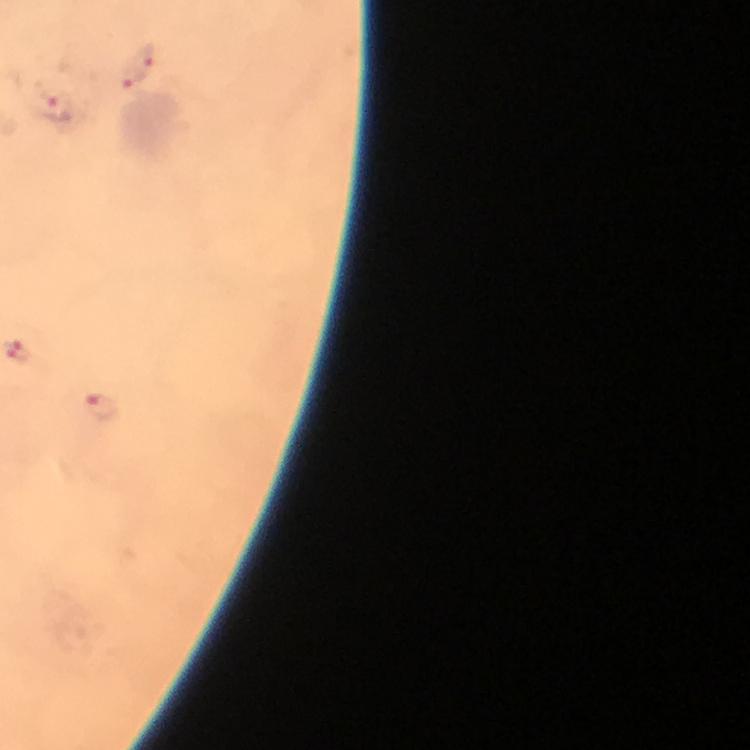
Approximate centers as [x, y] in pixels.
Summary:
  - Malaria parasite locations: [142, 59], [125, 80], [57, 107], [101, 407]
  - Immersion oil: used
  - Stain: Giemsa
  - Image size: 750×750 pixels
  - Magnification: 100x
  - Preparation: thick smear
  - Context: from a diagnostic examination for malaria
  - Capture: smartphone mounted on the microscope
  - Cropped from: one field of view